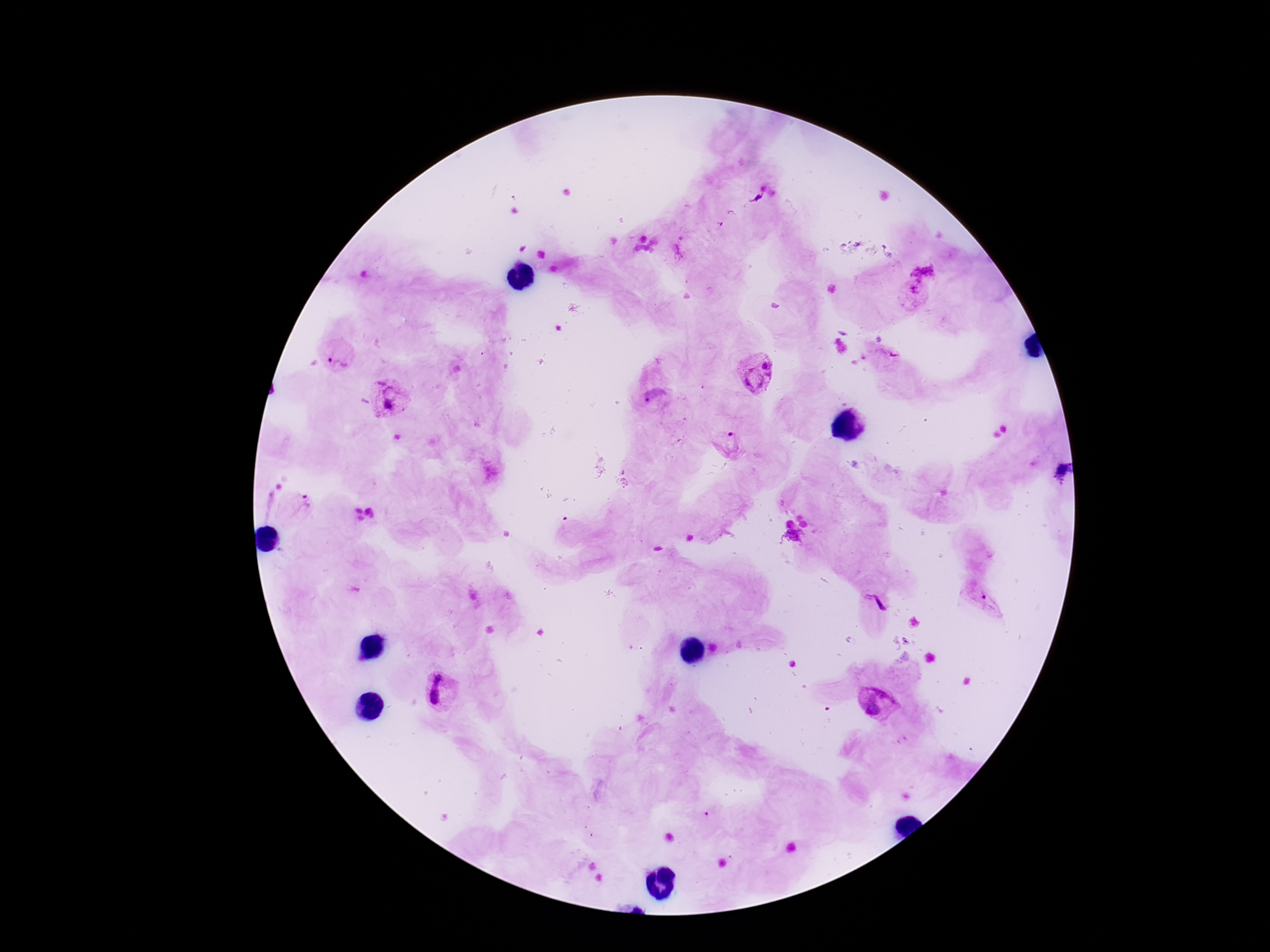
magnification = 100x
stain = Giemsa
field of view = single
Plasmodium parasite locations = approximate object centers, in pixels from the top-left corner: (x=922, y=273), (x=913, y=295), (x=337, y=356), (x=884, y=357), (x=755, y=373), (x=391, y=399), (x=655, y=399), (x=727, y=446), (x=299, y=504), (x=984, y=603), (x=441, y=690), (x=877, y=703)
patient malaria status = positive
image size = 1270×952 pixels
preparation = thick blood smear
capture = smartphone camera through the microscope eyepiece